Name the parasite shown.
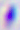
Toxoplasma gondii.

magnification = 400x
modality = micrograph